Classify this cell by malaria status.
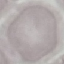
Uninfected.

Giemsa stain. Thin smear of blood. Photographed with a smartphone camera at the microscope eyepiece. Automatically extracted cell patch, resized to 64 × 64 pixels.